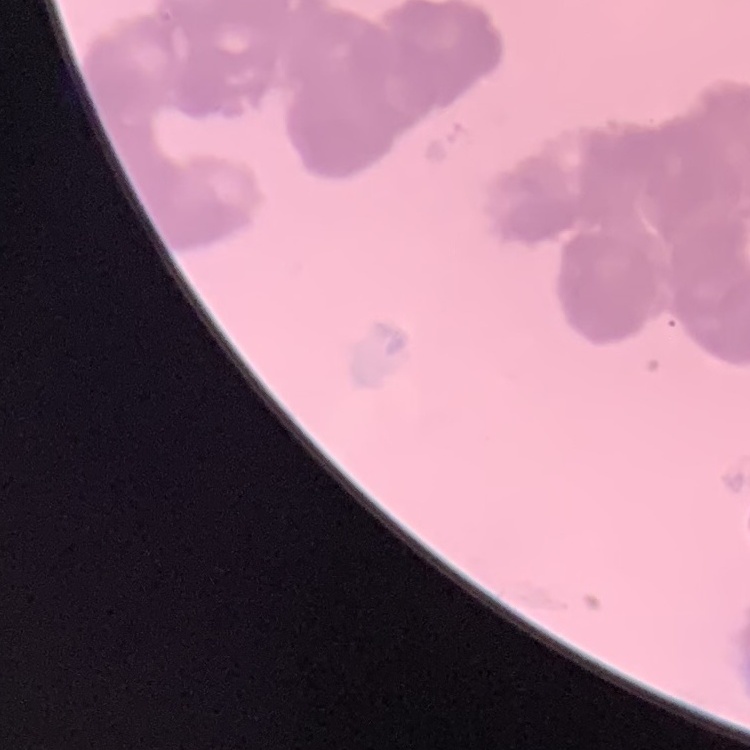

red blood cell morphology = rouleaux formation
preparation = thin blood smear
image type = one tile cut from a larger photomicrograph
stain = Field's or Giemsa